Outline each blood parasite and name the species.
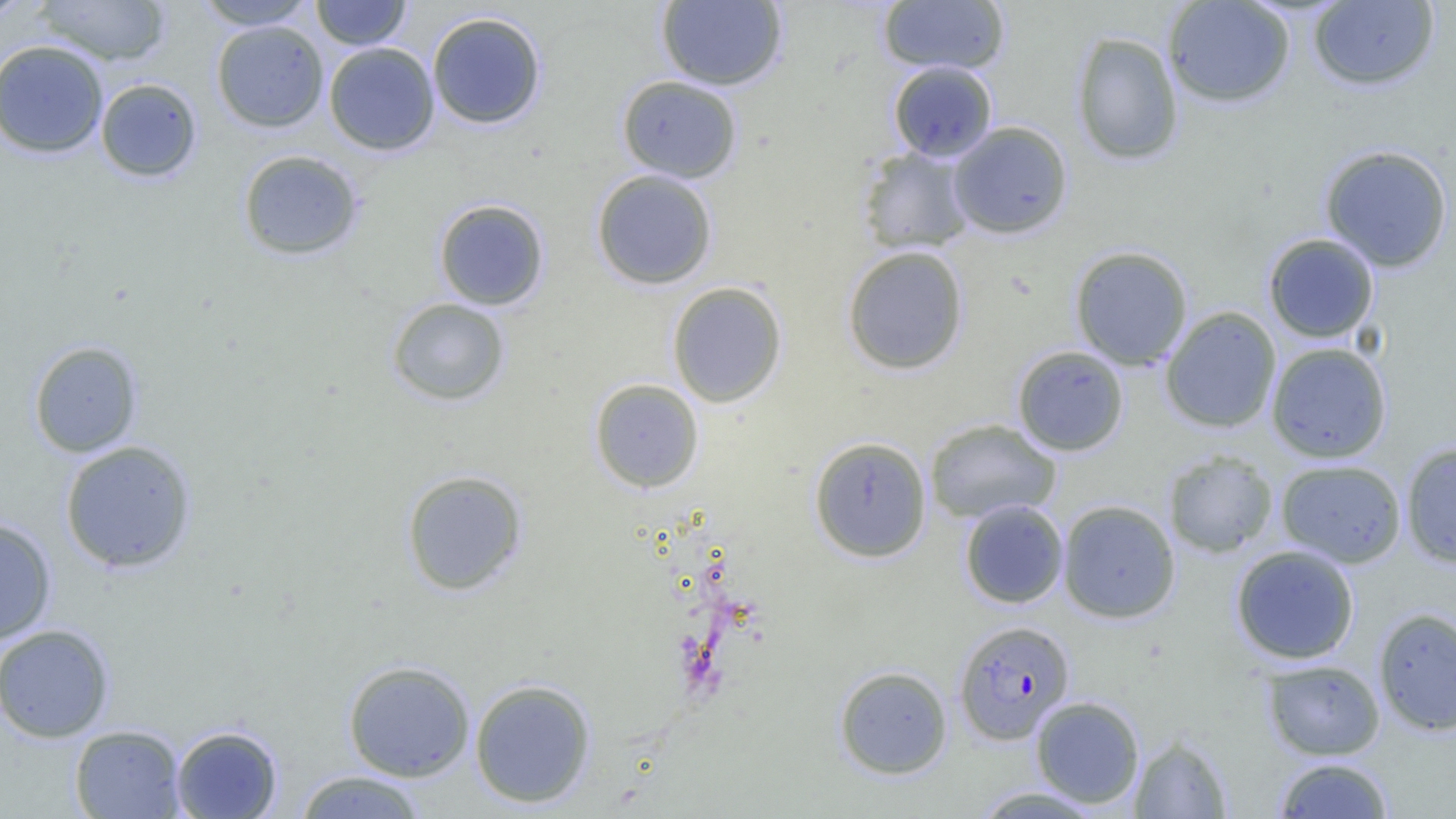
Approximate bounding boxes as [x1, y1, x2, y2] in pixels.
Plasmodium falciparum-infected red blood cells: [954, 620, 1075, 745].
No Plasmodium ovale, Plasmodium malariae, Plasmodium vivax, Babesia divergens, or Trypanosoma brucei observed.

Uninfected red blood cell locations: [0, 0, 32, 25], [33, 0, 172, 67], [194, 0, 317, 30], [311, 0, 412, 50], [877, 0, 1010, 75], [1162, 0, 1295, 108], [656, 1, 788, 90], [1308, 1, 1440, 91], [427, 11, 547, 130], [211, 20, 328, 133], [1070, 31, 1184, 166], [0, 40, 109, 158], [323, 42, 440, 156], [887, 61, 998, 163], [616, 75, 743, 183], [95, 78, 202, 183], [948, 121, 1073, 240], [1319, 144, 1453, 272], [857, 146, 976, 254], [237, 149, 364, 261], [591, 169, 718, 289], [433, 199, 550, 310], [1262, 233, 1380, 343], [842, 245, 969, 375], [1069, 245, 1193, 370], [667, 281, 787, 408], [386, 298, 510, 406], [1160, 307, 1282, 433], [28, 340, 143, 458], [1266, 342, 1392, 463], [1012, 345, 1129, 456], [590, 378, 704, 493], [924, 418, 1062, 524], [809, 436, 932, 562], [59, 440, 198, 574], [1400, 441, 1456, 568], [1163, 450, 1279, 558], [1276, 459, 1407, 568], [401, 469, 528, 596], [959, 499, 1069, 609], [1057, 499, 1181, 623], [0, 517, 57, 645], [1230, 544, 1360, 665], [1373, 607, 1456, 736], [0, 623, 115, 743], [343, 659, 475, 782], [1262, 659, 1385, 760], [834, 665, 953, 779], [470, 679, 596, 808], [1030, 695, 1145, 808], [69, 725, 187, 819], [170, 725, 283, 819], [1129, 734, 1232, 818], [1273, 756, 1395, 818], [293, 770, 429, 818], [970, 785, 1107, 818]. Slide-level diagnosis: Plasmodium falciparum. Optical microscopy. Image is 1456×819 pixels. Thin blood smear. Single field of view. Captured at 1000x magnification.